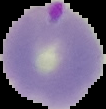
Summary:
  - Result: malaria parasites detected
  - Image type: cell region segmented out of the field of view; surrounding area masked to black
  - Preparation: thin blood smear
  - Image size: 106×109 pixels